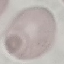
Malaria status: uninfected. Giemsa stain. Photographed with a smartphone camera at the microscope eyepiece. Thin blood film. Automatically extracted cell patch, resized to 64 × 64 pixels.